Give the extent of all Plasmodium ovale-infected red blood cells.
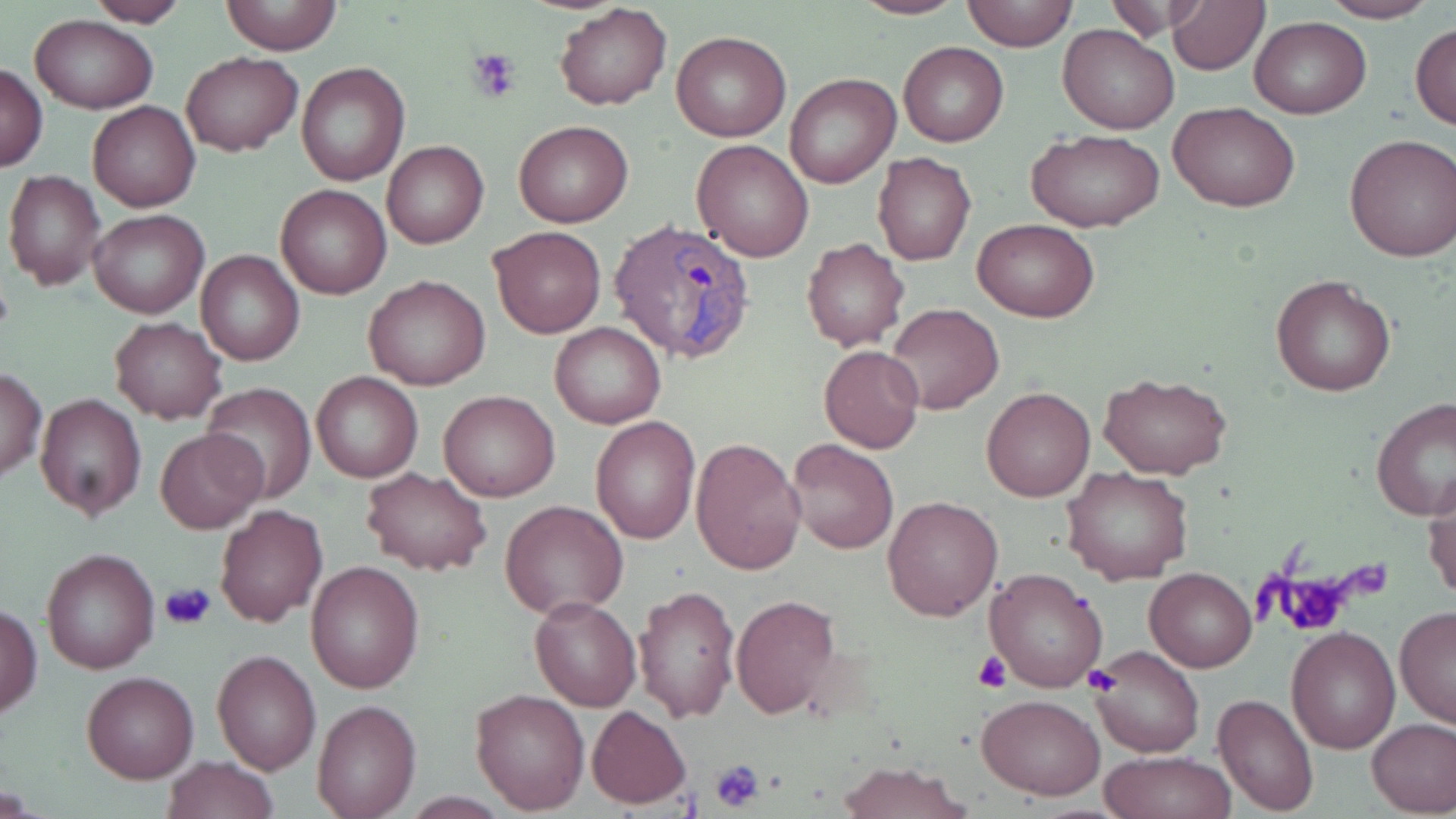
Approximate bounding boxes as named x1/y1/x2/y2 corners in pixels.
Plasmodium ovale-infected red blood cells: (x1=609, y1=220, x2=758, y2=363).

Platelet locations: (x1=469, y1=48, x2=522, y2=102), (x1=1274, y1=571, x2=1358, y2=636), (x1=160, y1=580, x2=217, y2=629), (x1=974, y1=652, x2=1012, y2=693), (x1=1084, y1=666, x2=1123, y2=695), (x1=708, y1=758, x2=767, y2=813). Uninfected red blood cell locations: (x1=220, y1=0, x2=342, y2=55), (x1=841, y1=0, x2=968, y2=19), (x1=962, y1=0, x2=1077, y2=50), (x1=1165, y1=0, x2=1269, y2=74), (x1=1317, y1=0, x2=1442, y2=23), (x1=83, y1=1, x2=189, y2=26), (x1=1104, y1=1, x2=1217, y2=40), (x1=554, y1=3, x2=672, y2=111), (x1=29, y1=15, x2=157, y2=114), (x1=1250, y1=16, x2=1369, y2=119), (x1=1410, y1=22, x2=1456, y2=129), (x1=1058, y1=24, x2=1179, y2=133), (x1=672, y1=29, x2=791, y2=142), (x1=898, y1=41, x2=1008, y2=147), (x1=181, y1=52, x2=302, y2=156), (x1=297, y1=62, x2=410, y2=186), (x1=0, y1=63, x2=48, y2=172), (x1=786, y1=73, x2=900, y2=190), (x1=88, y1=101, x2=200, y2=213), (x1=1170, y1=103, x2=1299, y2=212), (x1=513, y1=121, x2=633, y2=229), (x1=1026, y1=128, x2=1167, y2=234), (x1=1343, y1=133, x2=1455, y2=263), (x1=382, y1=139, x2=489, y2=249), (x1=692, y1=140, x2=815, y2=262), (x1=872, y1=152, x2=976, y2=266), (x1=4, y1=171, x2=106, y2=290), (x1=275, y1=184, x2=392, y2=299), (x1=88, y1=209, x2=209, y2=318), (x1=974, y1=218, x2=1097, y2=322), (x1=488, y1=226, x2=606, y2=338), (x1=802, y1=238, x2=910, y2=352), (x1=196, y1=248, x2=305, y2=366), (x1=1271, y1=274, x2=1397, y2=398), (x1=364, y1=275, x2=491, y2=391), (x1=883, y1=302, x2=1005, y2=415), (x1=109, y1=318, x2=227, y2=424), (x1=549, y1=322, x2=666, y2=429), (x1=820, y1=345, x2=925, y2=454), (x1=0, y1=369, x2=45, y2=480), (x1=1097, y1=370, x2=1234, y2=478), (x1=311, y1=372, x2=423, y2=483), (x1=202, y1=383, x2=316, y2=504), (x1=981, y1=387, x2=1095, y2=502), (x1=439, y1=390, x2=560, y2=502), (x1=35, y1=392, x2=148, y2=520), (x1=1372, y1=398, x2=1456, y2=520), (x1=591, y1=416, x2=700, y2=543), (x1=155, y1=427, x2=267, y2=533), (x1=691, y1=437, x2=807, y2=577), (x1=786, y1=437, x2=898, y2=555), (x1=1063, y1=466, x2=1192, y2=587), (x1=362, y1=467, x2=491, y2=576), (x1=1423, y1=474, x2=1456, y2=604), (x1=882, y1=494, x2=1003, y2=621), (x1=502, y1=500, x2=628, y2=618), (x1=214, y1=503, x2=328, y2=627), (x1=41, y1=547, x2=161, y2=674), (x1=305, y1=560, x2=424, y2=694), (x1=985, y1=566, x2=1109, y2=693), (x1=1145, y1=568, x2=1256, y2=672), (x1=634, y1=583, x2=739, y2=723), (x1=530, y1=596, x2=641, y2=710), (x1=733, y1=596, x2=841, y2=719), (x1=1, y1=603, x2=42, y2=720), (x1=1395, y1=606, x2=1456, y2=730), (x1=1285, y1=626, x2=1399, y2=754), (x1=1087, y1=645, x2=1205, y2=757), (x1=212, y1=649, x2=319, y2=774), (x1=81, y1=671, x2=199, y2=782), (x1=470, y1=688, x2=591, y2=813), (x1=1214, y1=691, x2=1318, y2=814), (x1=976, y1=693, x2=1105, y2=800), (x1=311, y1=698, x2=422, y2=818), (x1=586, y1=705, x2=691, y2=810), (x1=1367, y1=717, x2=1456, y2=816), (x1=1100, y1=751, x2=1237, y2=819), (x1=161, y1=755, x2=280, y2=819), (x1=836, y1=760, x2=970, y2=818). Slide-level diagnosis: Plasmodium ovale. May-Grünwald-Giemsa stain. Thin blood film. Image is 1456×819 pixels. Optical microscopy. One field of a larger specimen. Captured at 1000x magnification.